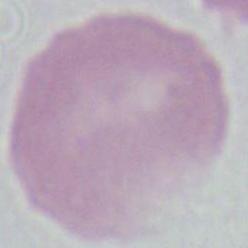
Summary:
  - Modality: micrograph
  - Identification: erythrocyte
  - Magnification: 1000x